State the blood parasite species.
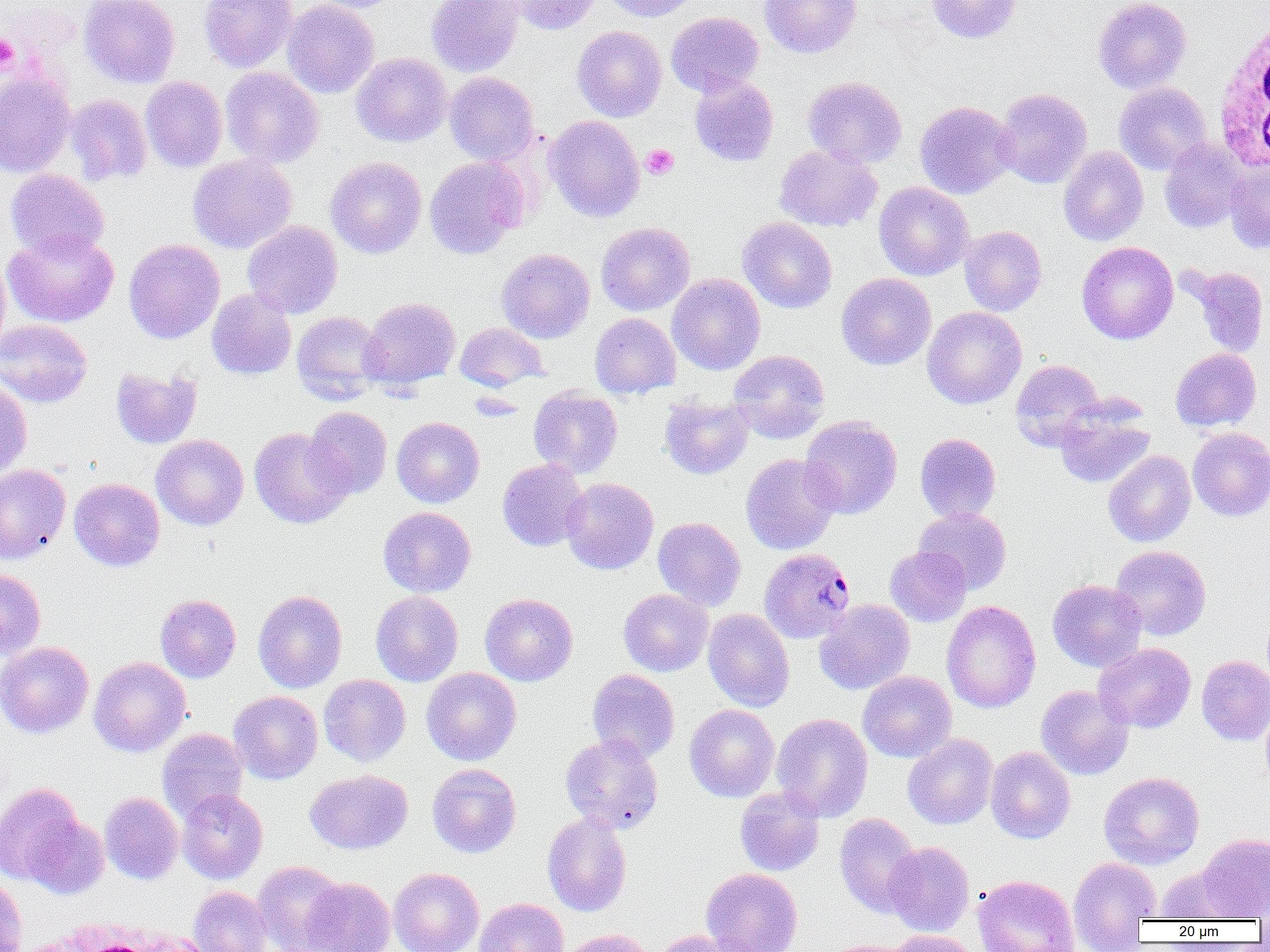
Plasmodium malariae.

modality: light microscopy
field_of_view: one of a larger specimen
preparation: thin blood smear
magnification: 1000x
plasmodium_malariae_infected_red_blood_cell_locations: 'approximate bounding boxes as [x1, y1, x2, y2] in pixels: [758, 547, 855, 643]'
image_size: 1270×952 pixels
white_blood_cell_locations: 'approximate bounding boxes as [x1, y1, x2, y2] in pixels: [1212, 14, 1269, 176], [36, 917, 211, 951]'
platelet_locations: 'approximate bounding boxes as [x1, y1, x2, y2] in pixels: [0, 34, 19, 72], [641, 144, 679, 180]'
uninfected_red_blood_cell_locations: 'approximate bounding boxes as [x1, y1, x2, y2] in pixels: [79, 0, 180, 88], [198, 0, 298, 72], [282, 0, 379, 98], [309, 0, 403, 13], [426, 0, 523, 77], [507, 0, 603, 35], [602, 0, 700, 22], [759, 0, 862, 58], [926, 0, 1021, 43], [1093, 0, 1191, 94], [665, 11, 764, 97], [572, 25, 667, 122], [351, 53, 452, 147], [220, 66, 324, 168], [0, 72, 75, 178], [444, 72, 539, 166], [689, 75, 778, 166], [140, 76, 228, 172], [803, 76, 907, 168], [1114, 82, 1212, 175], [994, 87, 1092, 188], [65, 94, 152, 185], [915, 101, 1016, 199], [545, 114, 645, 222], [1160, 138, 1247, 233], [774, 144, 882, 232], [1059, 146, 1148, 246], [187, 154, 297, 254], [326, 156, 427, 258], [424, 156, 528, 259], [1225, 161, 1270, 253], [5, 169, 109, 259], [874, 182, 974, 281], [738, 217, 837, 313], [242, 220, 342, 318], [596, 222, 695, 316], [959, 225, 1047, 316], [3, 228, 119, 328], [123, 238, 224, 344], [1076, 241, 1178, 344], [496, 248, 595, 343], [0, 254, 11, 358], [1185, 266, 1269, 358], [667, 273, 766, 375], [836, 273, 936, 370], [206, 288, 296, 379], [360, 296, 461, 390], [922, 306, 1026, 409], [292, 311, 386, 403], [590, 312, 681, 398], [0, 319, 92, 407], [455, 322, 548, 391], [1170, 348, 1262, 432], [728, 349, 830, 443], [1010, 359, 1106, 449], [110, 366, 202, 449], [0, 381, 32, 480], [528, 386, 623, 479], [659, 396, 754, 480], [1054, 401, 1155, 489], [304, 406, 392, 499], [800, 415, 902, 519], [392, 417, 484, 507], [249, 427, 352, 529], [1187, 427, 1270, 521], [915, 433, 1000, 523], [151, 435, 249, 531], [1103, 450, 1195, 547], [741, 453, 841, 555], [497, 459, 588, 551], [0, 464, 70, 562], [562, 477, 658, 574], [69, 478, 165, 571], [378, 506, 476, 597], [913, 507, 1012, 594], [652, 517, 746, 610], [1110, 545, 1212, 640], [885, 546, 972, 627], [0, 568, 46, 659], [1047, 579, 1147, 672], [618, 588, 713, 677], [253, 590, 347, 693], [370, 591, 463, 686], [155, 593, 241, 683], [479, 593, 578, 686], [814, 599, 915, 695], [941, 600, 1041, 714], [703, 608, 794, 712], [0, 641, 93, 738], [1093, 643, 1196, 733], [1197, 656, 1270, 745], [89, 657, 191, 757], [421, 667, 521, 765], [587, 670, 680, 763], [857, 670, 956, 763], [318, 674, 410, 766], [1035, 685, 1134, 780], [228, 691, 323, 784], [1260, 703, 1270, 791], [684, 704, 780, 802], [772, 713, 873, 822], [157, 728, 248, 820], [560, 733, 664, 834], [902, 734, 998, 830], [986, 746, 1075, 844], [427, 764, 521, 858], [304, 769, 413, 854], [1099, 772, 1205, 870], [0, 782, 83, 885], [734, 786, 825, 876], [177, 788, 268, 884], [100, 792, 183, 884], [542, 812, 632, 916], [834, 813, 923, 917], [25, 815, 109, 899], [1198, 833, 1270, 919], [884, 841, 974, 936], [1068, 857, 1161, 949], [253, 861, 345, 952], [1155, 865, 1247, 921], [389, 867, 484, 952], [701, 867, 803, 952], [973, 875, 1078, 952], [0, 877, 27, 952], [298, 877, 395, 951], [187, 886, 273, 952], [474, 897, 568, 952], [559, 929, 653, 952], [650, 930, 757, 952], [884, 930, 982, 952], [821, 939, 920, 952]'